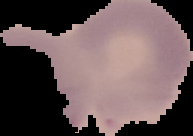 From a thin blood smear. Image is 193×136 pixels. Malaria status: uninfected. Cell region segmented out of the field of view; the surrounding area is masked to black.